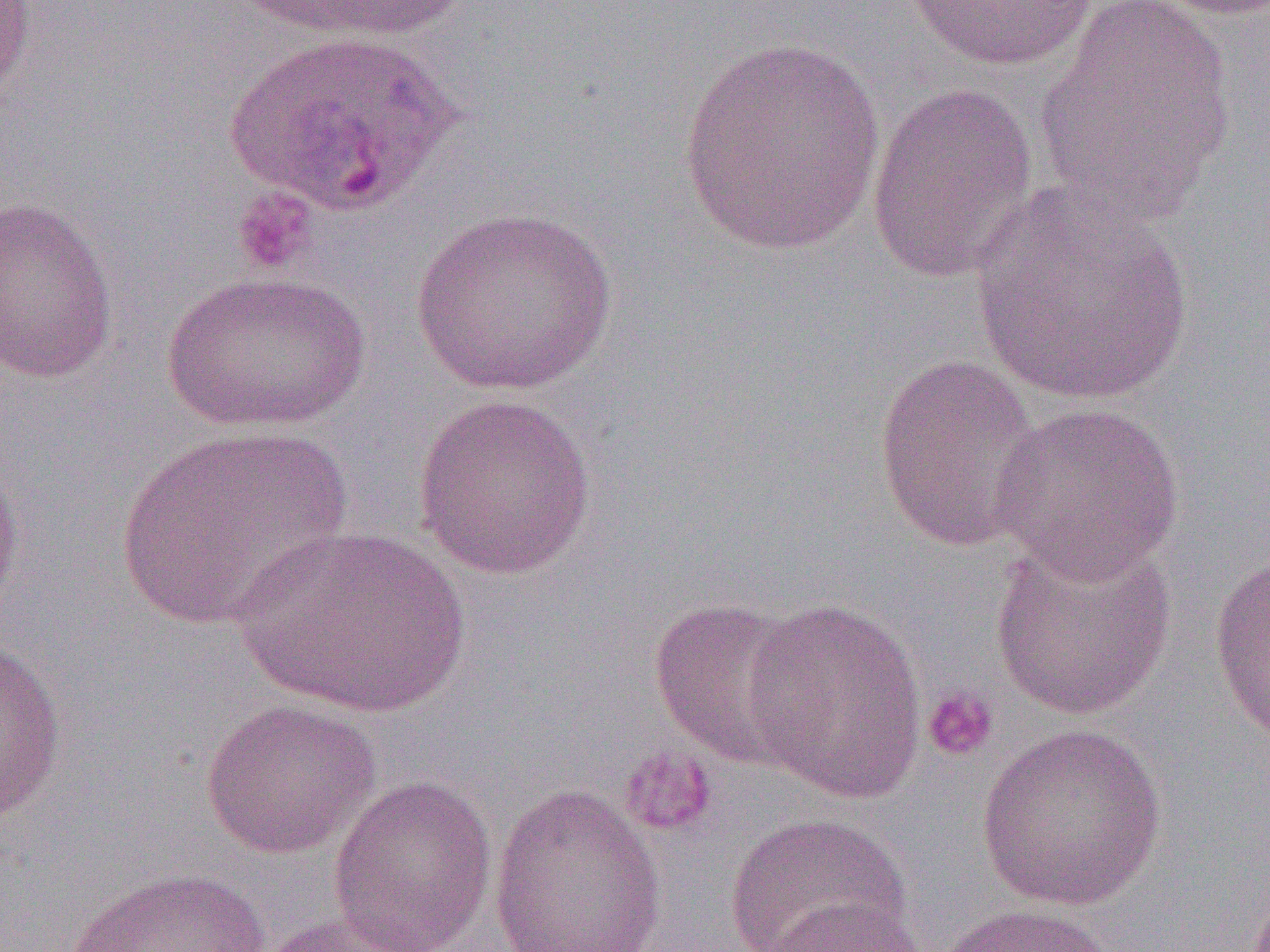

{
  "slide_level_diagnosis": "Plasmodium ovale",
  "platelet_locations": "approximate bounding boxes as named x1/y1/x2/y2 corners in pixels: (x1=231, y1=186, x2=321, y2=276), (x1=921, y1=685, x2=1000, y2=762), (x1=618, y1=747, x2=718, y2=838)",
  "magnification": "1000x",
  "image_size": "1270×952 pixels",
  "uninfected_red_blood_cell_locations": "approximate bounding boxes as named x1/y1/x2/y2 corners in pixels: (x1=0, y1=0, x2=38, y2=106), (x1=1138, y1=0, x2=1270, y2=20), (x1=256, y1=1, x2=473, y2=42), (x1=901, y1=1, x2=1102, y2=71), (x1=1032, y1=1, x2=1238, y2=224), (x1=224, y1=29, x2=458, y2=215), (x1=676, y1=36, x2=888, y2=254), (x1=866, y1=83, x2=1039, y2=285), (x1=974, y1=184, x2=1194, y2=406), (x1=0, y1=195, x2=119, y2=384), (x1=410, y1=206, x2=620, y2=395), (x1=157, y1=270, x2=370, y2=435), (x1=872, y1=353, x2=1044, y2=552), (x1=411, y1=393, x2=598, y2=580), (x1=989, y1=402, x2=1185, y2=584), (x1=114, y1=426, x2=354, y2=630), (x1=0, y1=444, x2=26, y2=616), (x1=228, y1=525, x2=473, y2=719), (x1=987, y1=533, x2=1180, y2=722), (x1=1208, y1=549, x2=1270, y2=745), (x1=739, y1=596, x2=930, y2=804), (x1=648, y1=598, x2=812, y2=769), (x1=0, y1=640, x2=68, y2=826), (x1=199, y1=698, x2=381, y2=859), (x1=974, y1=722, x2=1167, y2=911), (x1=327, y1=774, x2=498, y2=952), (x1=486, y1=781, x2=669, y2=952), (x1=724, y1=812, x2=912, y2=952), (x1=63, y1=866, x2=277, y2=952), (x1=755, y1=896, x2=926, y2=952), (x1=929, y1=902, x2=1120, y2=952), (x1=248, y1=912, x2=429, y2=952)",
  "field_of_view": "single",
  "modality": "optical microscopy",
  "preparation": "thin blood film"
}